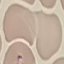
malaria_status: parasitized
preparation: thin blood smear
stain: Giemsa
image_type: automatically extracted cell patch, resized to 64 × 64 pixels
capture: smartphone camera at the microscope eyepiece